Name the parasite shown.
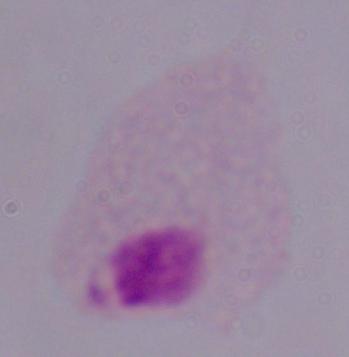
A trichomonad.

Summary:
  - Magnification: 1000x
  - Modality: photomicrograph